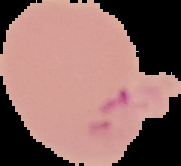

Image is 181×166 pixels. Result: Plasmodium parasites detected. Cell region segmented out of the field of view; the surrounding area is masked to black. From a thin blood smear.